Identify the parasite.
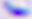

Toxoplasma gondii.

Photomicrograph. 400x magnification.